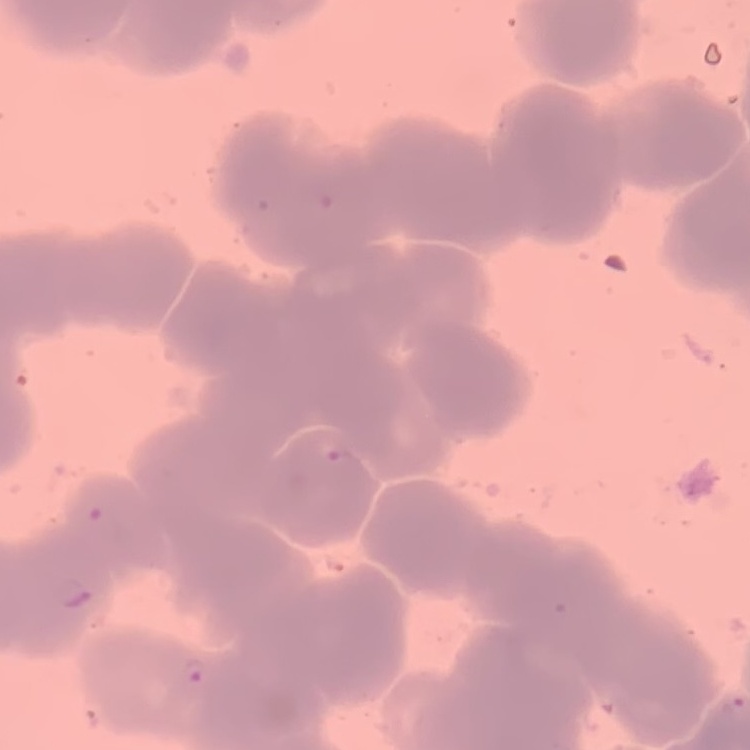

Summary:
  - Red blood cell morphology: rouleaux formation
  - Stain: Field's or Giemsa
  - Image type: square crop of a larger photomicrograph
  - Preparation: thin peripheral smear